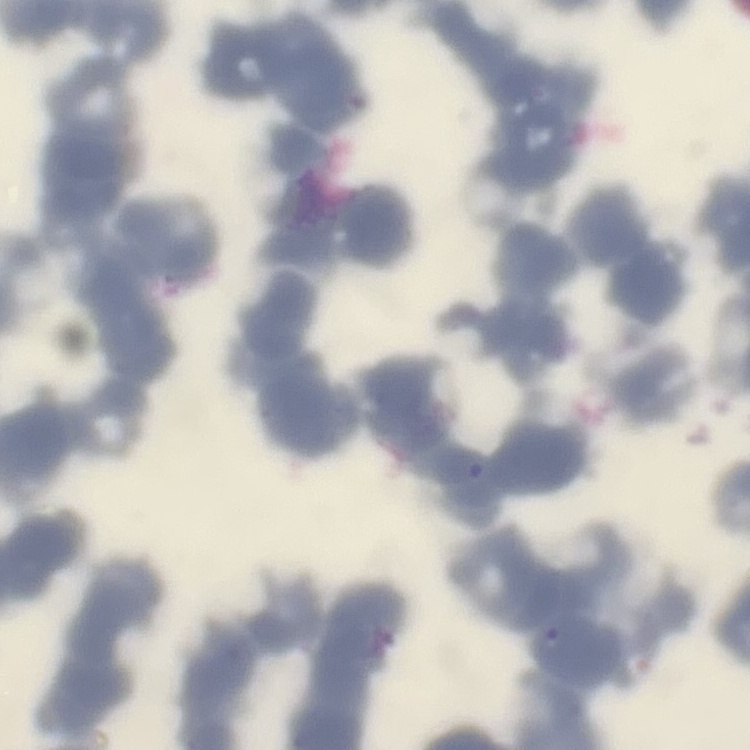

erythrocyte morphology = rouleaux formation
preparation = thin peripheral smear
image type = one tile cut from a larger photomicrograph
stain = Field's or Giemsa